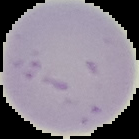

Image is 139×139 pixels. Cell region segmented out of the field of view; the surrounding area is masked to black. Malaria status: uninfected. From a thin blood smear.